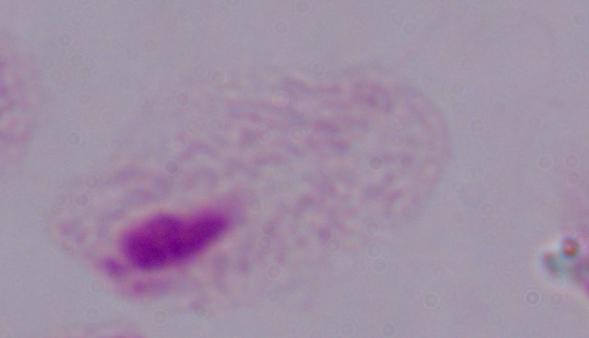

Captured at 1000x magnification. Micrograph. A trichomonad is shown.